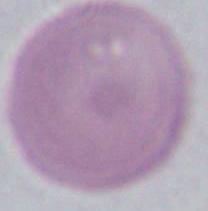

Summary:
  - Modality: micrograph
  - Identification: red blood cell
  - Magnification: 1000x